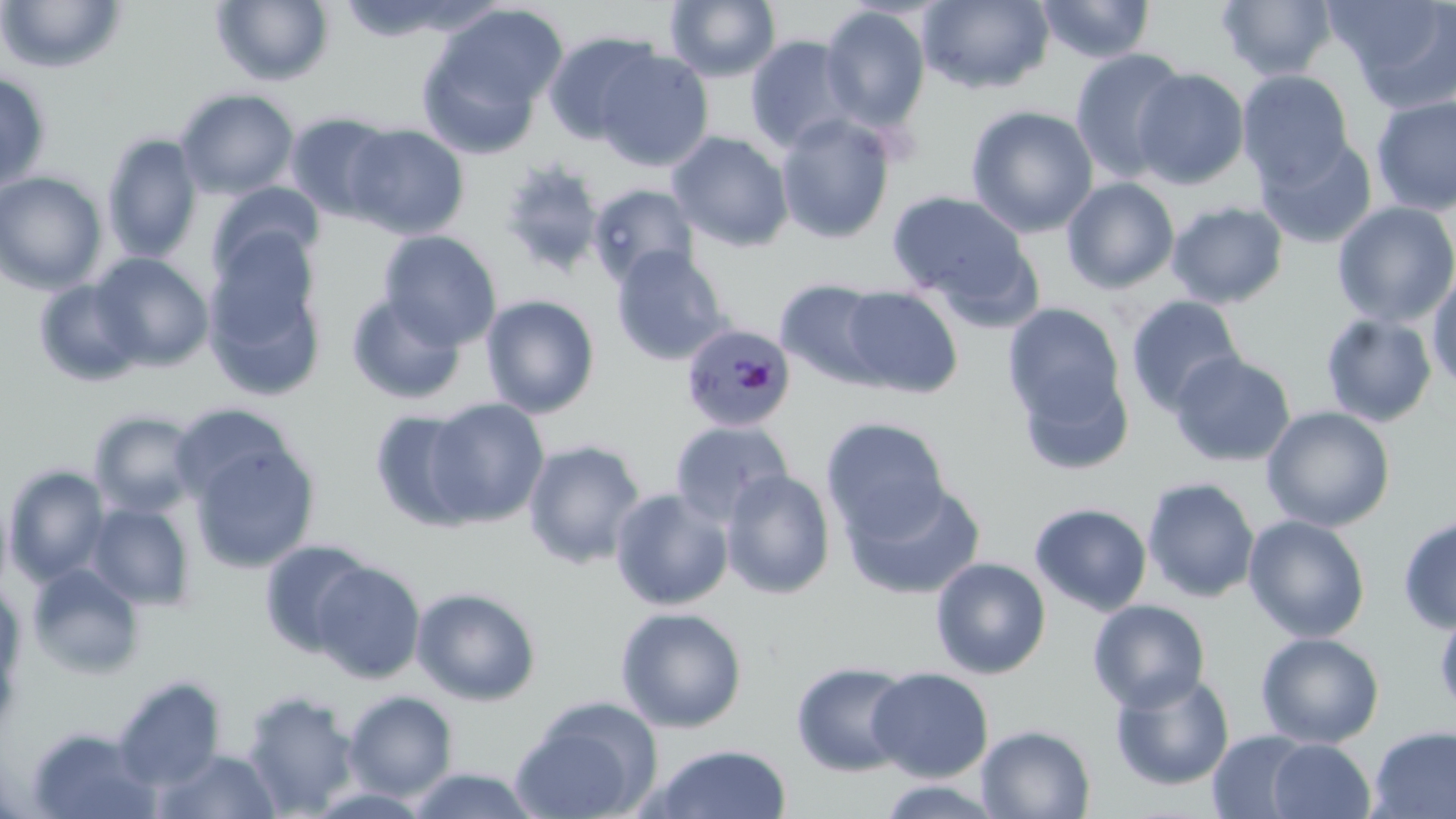
Summary:
  - Coordinate format: approximate bounding boxes as [x1, y1, x2, y2] in pixels
  - Plasmodium malariae-infected red blood cell locations: [680, 323, 796, 432]
  - Uninfected red blood cell locations: [212, 0, 334, 86], [664, 0, 782, 82], [918, 0, 1055, 94], [1036, 0, 1155, 64], [1217, 0, 1338, 81], [1327, 0, 1456, 112], [0, 1, 126, 74], [429, 3, 568, 121], [820, 5, 931, 134], [543, 31, 664, 144], [744, 35, 861, 154], [416, 38, 546, 159], [593, 48, 714, 172], [1070, 48, 1191, 181], [1132, 68, 1250, 189], [1238, 70, 1354, 189], [0, 72, 51, 192], [175, 88, 299, 199], [1370, 95, 1456, 216], [965, 104, 1099, 237], [285, 112, 398, 222], [775, 114, 895, 244], [343, 123, 469, 239], [668, 131, 794, 251], [102, 133, 203, 264], [1256, 136, 1378, 249], [498, 158, 606, 278], [0, 171, 107, 294], [1062, 176, 1179, 294], [207, 182, 324, 282], [587, 183, 700, 287], [887, 190, 1030, 306], [1166, 201, 1289, 309], [1331, 201, 1456, 328], [378, 230, 501, 349], [202, 242, 327, 403], [610, 247, 729, 365], [90, 253, 213, 371], [1427, 264, 1456, 395], [34, 278, 146, 387], [775, 278, 896, 388], [839, 286, 964, 398], [346, 293, 467, 405], [480, 295, 600, 418], [1125, 295, 1245, 416], [1003, 302, 1129, 442], [1320, 313, 1438, 427], [1169, 351, 1296, 467], [1014, 361, 1135, 476], [421, 397, 551, 527], [172, 404, 297, 507], [1261, 406, 1396, 532], [369, 408, 483, 531], [89, 411, 204, 519], [821, 417, 951, 541], [670, 420, 793, 526], [188, 440, 320, 572], [522, 440, 647, 570], [5, 466, 110, 585], [720, 468, 836, 599], [1141, 477, 1260, 602], [842, 480, 987, 599], [609, 488, 734, 610], [1029, 502, 1152, 616], [85, 503, 195, 610], [1243, 514, 1370, 642], [1397, 514, 1456, 633], [259, 539, 376, 657], [930, 557, 1051, 679], [311, 560, 425, 684], [26, 563, 145, 680], [411, 586, 542, 706], [1088, 599, 1211, 713], [1433, 605, 1456, 721], [615, 606, 748, 732], [1255, 631, 1385, 749], [791, 661, 915, 777], [866, 667, 993, 782], [1110, 671, 1235, 791], [114, 678, 225, 790], [343, 690, 458, 801], [242, 691, 359, 816], [511, 698, 661, 819], [976, 724, 1096, 818], [1367, 725, 1456, 818], [25, 728, 164, 818], [1207, 730, 1319, 817], [1266, 738, 1375, 818], [647, 744, 793, 819], [153, 748, 282, 818], [405, 767, 542, 819], [873, 779, 1007, 818]
  - Slide-level diagnosis: Plasmodium malariae
  - Magnification: 1000x
  - Stain: May-Grünwald-Giemsa
  - Preparation: thin blood film
  - Image size: 1456×819 pixels
  - Field of view: one of a larger specimen
  - Modality: optical microscopy